Describe the morphology of the erythrocytes.
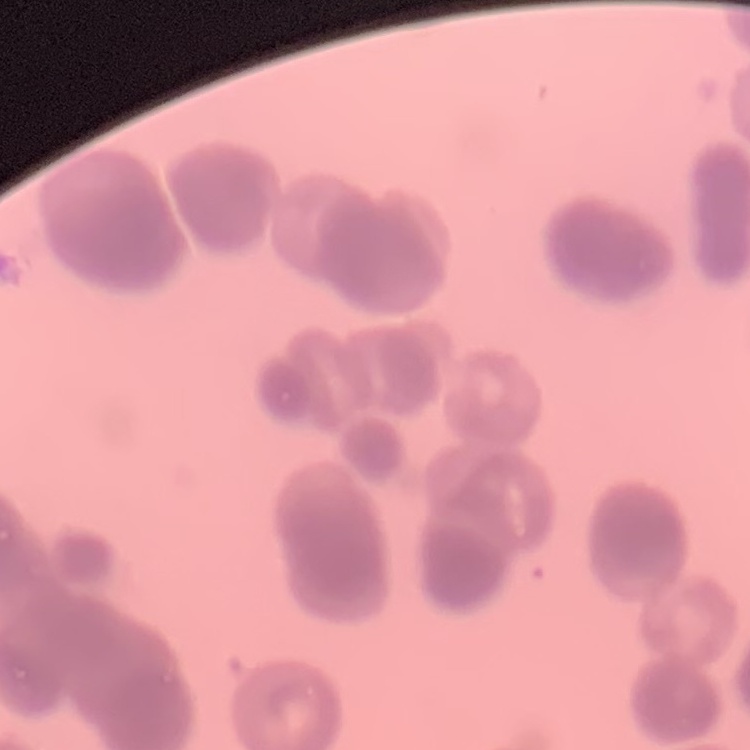
Rouleaux formation.

Field's or Giemsa stain. Square crop of a larger photomicrograph. Thin blood smear.